Assess this cell for malaria.
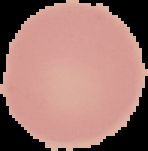
Uninfected.

Image is 148×151 pixels. From a thin blood film. Cell region segmented out of the field of view; the surrounding area is masked to black.